Outline each blood parasite and name the species.
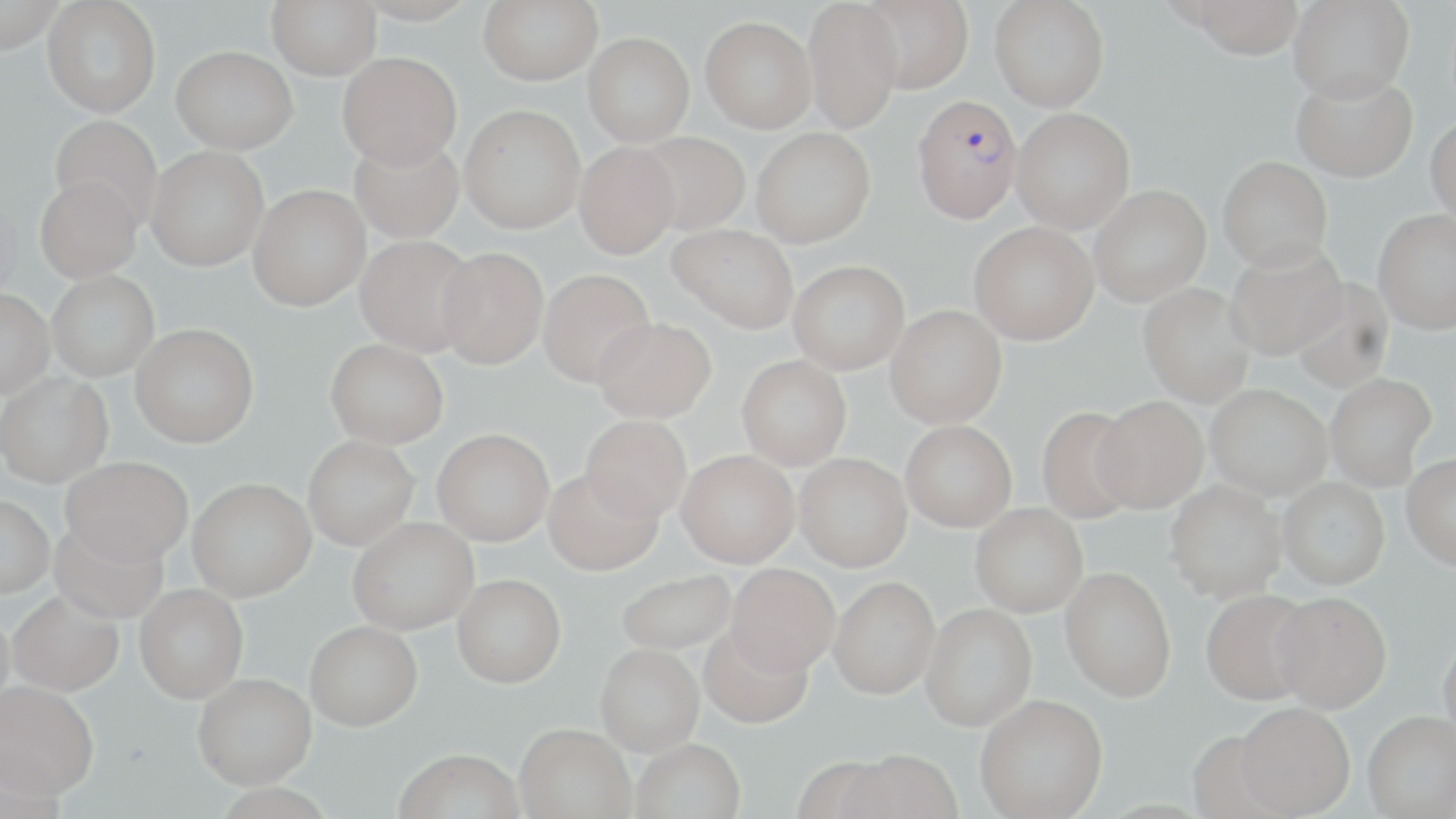

Approximate bounding boxes as (x1, y1, x2, y2) in pixels.
Plasmodium falciparum-infected red blood cells: (912, 95, 1022, 223).
No Plasmodium ovale, Plasmodium malariae, Plasmodium vivax, Babesia divergens, or Trypanosoma brucei observed.

Uninfected red blood cell locations: (0, 0, 66, 54), (42, 0, 161, 117), (267, 0, 381, 79), (355, 0, 479, 25), (478, 0, 603, 86), (858, 0, 973, 94), (989, 0, 1109, 112), (1183, 0, 1305, 59), (802, 1, 903, 133), (1287, 1, 1415, 102), (700, 16, 817, 133), (583, 32, 694, 146), (171, 45, 298, 154), (337, 51, 462, 169), (1291, 72, 1417, 183), (459, 104, 585, 234), (1011, 107, 1135, 233), (49, 115, 163, 230), (1425, 115, 1456, 228), (751, 128, 875, 247), (633, 131, 750, 235), (349, 134, 464, 243), (574, 142, 679, 259), (146, 146, 269, 271), (1218, 156, 1333, 271), (35, 174, 142, 282), (248, 184, 370, 311), (1089, 184, 1210, 306), (1372, 209, 1456, 333), (969, 222, 1098, 345), (668, 224, 798, 333), (355, 235, 478, 355), (1225, 243, 1349, 360), (436, 246, 548, 368), (788, 260, 909, 374), (538, 268, 655, 387), (47, 270, 159, 381), (1290, 277, 1394, 392), (1137, 283, 1256, 408), (0, 290, 54, 399), (885, 304, 1007, 428), (592, 317, 715, 423), (131, 323, 258, 448), (325, 339, 449, 448), (737, 355, 851, 470), (0, 372, 113, 490), (1325, 373, 1437, 490), (1205, 385, 1331, 500), (1093, 396, 1208, 513), (1036, 406, 1140, 524), (580, 415, 691, 524), (900, 420, 1016, 531), (433, 430, 554, 546), (303, 436, 419, 551), (676, 450, 800, 568), (1401, 453, 1456, 570), (794, 454, 912, 572), (60, 457, 193, 568), (543, 469, 663, 578), (1278, 477, 1390, 590), (1165, 479, 1287, 601), (187, 480, 316, 604), (0, 497, 54, 600), (970, 504, 1088, 618), (47, 519, 169, 625), (348, 519, 479, 636), (726, 565, 839, 677), (1060, 568, 1176, 703), (616, 570, 737, 656), (451, 578, 565, 691), (828, 579, 940, 702), (134, 586, 247, 705), (1201, 589, 1318, 706), (7, 592, 124, 699), (1271, 592, 1392, 713), (920, 605, 1037, 734), (0, 612, 15, 725), (305, 623, 422, 734), (699, 626, 813, 732), (1438, 628, 1456, 746), (596, 648, 704, 759), (192, 677, 317, 794), (0, 685, 99, 807), (975, 697, 1108, 819), (1234, 703, 1355, 818), (1363, 712, 1456, 818), (515, 728, 636, 819), (631, 742, 746, 819), (394, 753, 525, 819), (839, 753, 964, 819), (211, 786, 338, 819). Slide-level diagnosis: Plasmodium falciparum. Light microscopy. Captured at 1000x magnification. Image is 1456×819 pixels. Single field of view. May-Grünwald-Giemsa-stained preparation. Thin blood film.